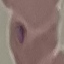
Summary:
  - Malaria status: parasitized
  - Capture: smartphone through the microscope eyepiece
  - Preparation: thin blood smear
  - Stain: Giemsa
  - Image type: cell patch, automatically extracted from a larger field of view and resized to 64 × 64 pixels